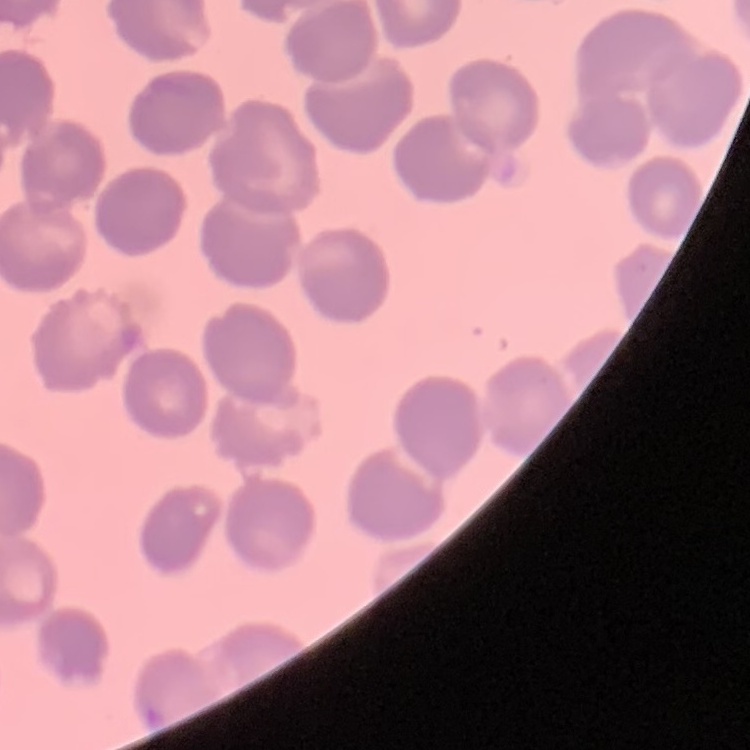 The erythrocytes exhibit no rouleaux formation. Thin blood smear. Stained with either Field's or Giemsa. One tile cut from a larger photomicrograph.